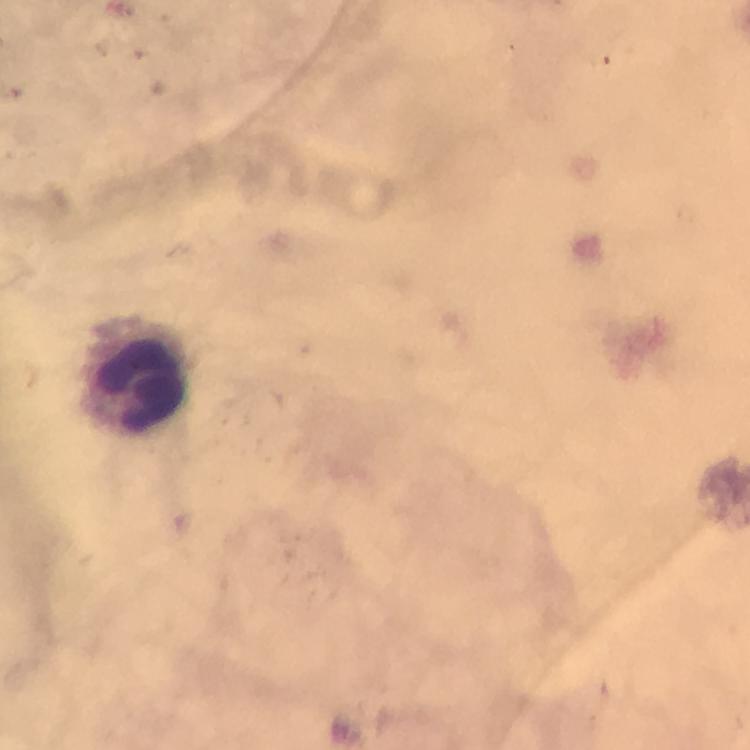

Approximate centers as (x, y) in pixels.
Summary:
  - Leukocyte locations: (142, 373)
  - Capture: smartphone camera through the microscope
  - Preparation: thick blood smear
  - Stain: Giemsa
  - Cropped from: one field of view
  - Image size: 750×750 pixels
  - Magnification: 100x
  - Immersion oil: used
  - Context: from a diagnostic examination for malaria
  - Plasmodium parasites: none detected